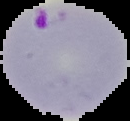

From a thin blood smear. Cell region segmented out of the field of view; the surrounding area is masked to black. Image is 130×121 pixels. Result: malaria parasites detected.